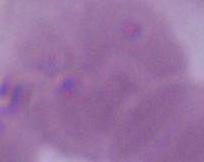
A red blood cell is seen. Captured at 1000x magnification. Photomicrograph.